Name the cell type shown.
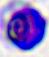

A leukocyte.

Captured at 400x magnification. Photomicrograph.